Look for Plasmodium parasites.
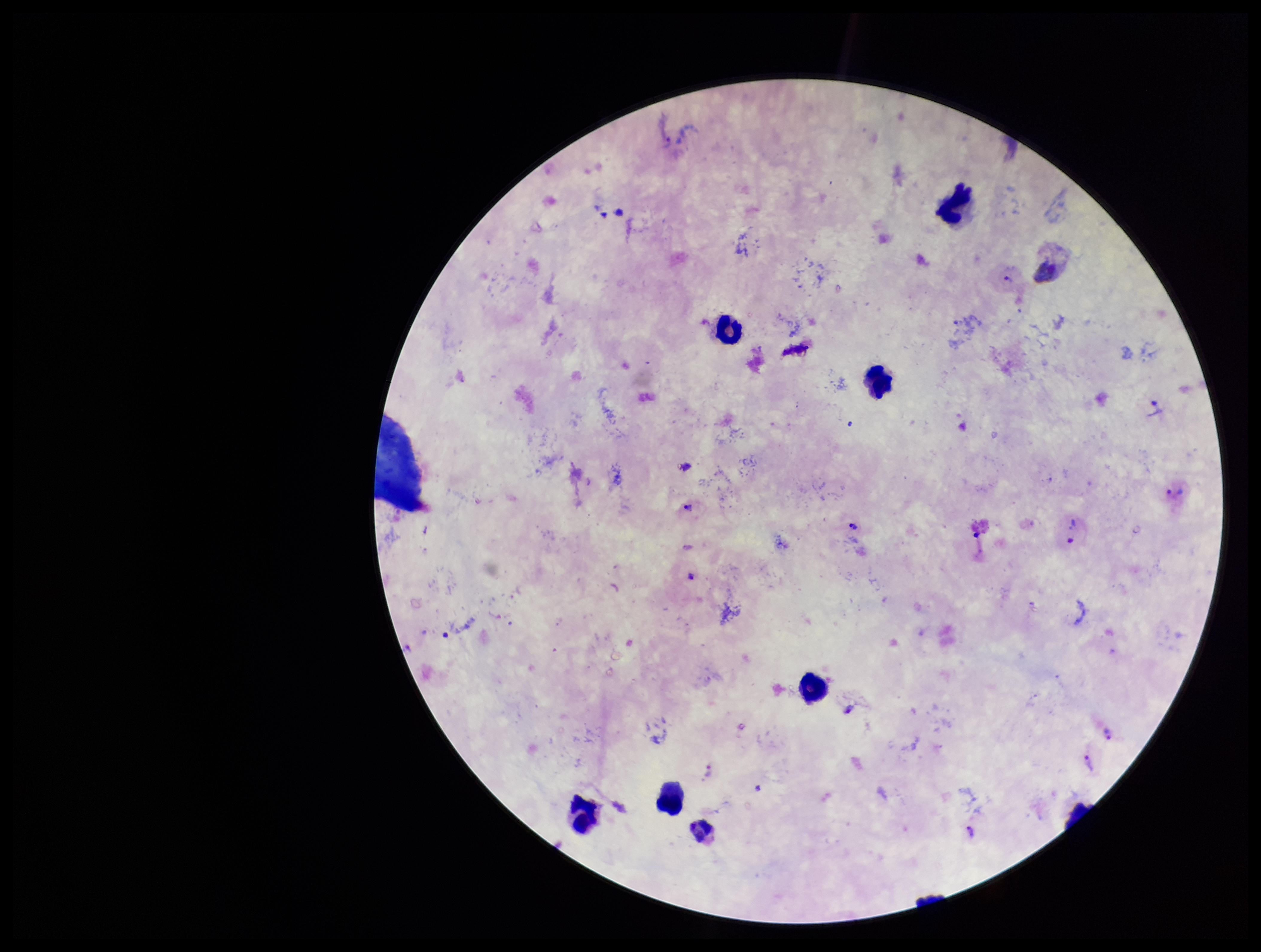
Identified.

Giemsa stain. Leukocyte count: 7. Photographed through the microscope eyepiece with a smartphone camera. Preparation: thick blood smear. Patient malaria status: positive. Parasite count: 7. Image is 1261×952 pixels. Species reported for this patient: Plasmodium vivax. Single field of view.